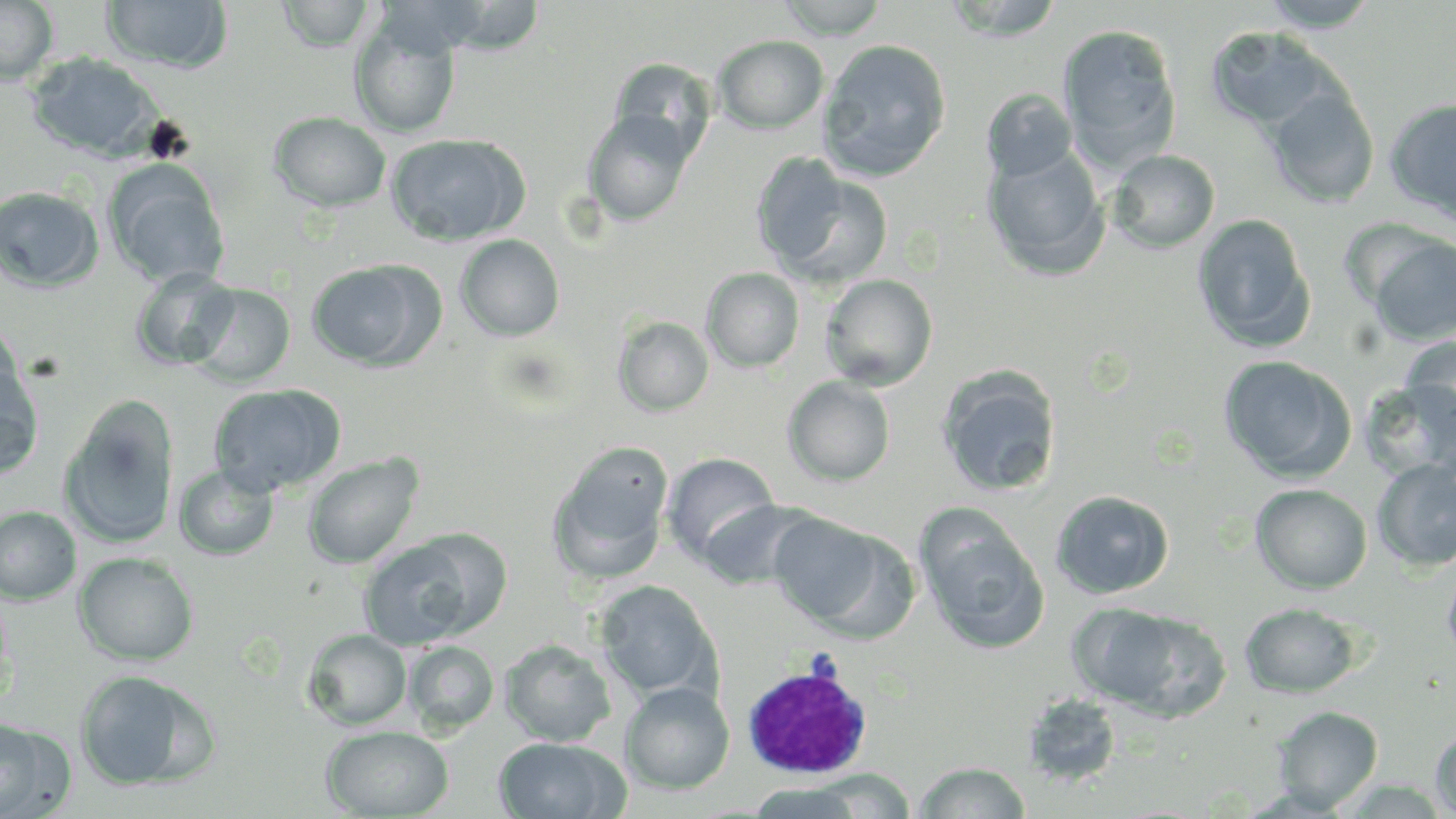

Summary:
  - Coordinate format: approximate bounding boxes as named x1/y1/x2/y2 corners in pixels
  - White blood cell locations: (x1=739, y1=661, x2=876, y2=779)
  - Uninfected red blood cell locations: (x1=0, y1=0, x2=59, y2=87), (x1=775, y1=0, x2=890, y2=39), (x1=940, y1=0, x2=1066, y2=41), (x1=1256, y1=0, x2=1383, y2=32), (x1=100, y1=1, x2=234, y2=73), (x1=277, y1=1, x2=376, y2=52), (x1=349, y1=15, x2=461, y2=138), (x1=1058, y1=23, x2=1182, y2=170), (x1=1206, y1=27, x2=1341, y2=132), (x1=712, y1=35, x2=829, y2=134), (x1=817, y1=38, x2=952, y2=182), (x1=26, y1=53, x2=164, y2=161), (x1=607, y1=58, x2=718, y2=164), (x1=1265, y1=87, x2=1379, y2=209), (x1=982, y1=88, x2=1078, y2=183), (x1=1384, y1=96, x2=1456, y2=224), (x1=583, y1=110, x2=696, y2=227), (x1=268, y1=111, x2=392, y2=212), (x1=385, y1=133, x2=529, y2=246), (x1=983, y1=147, x2=1110, y2=279), (x1=1107, y1=149, x2=1220, y2=253), (x1=752, y1=157, x2=892, y2=290), (x1=104, y1=160, x2=230, y2=288), (x1=0, y1=185, x2=105, y2=292), (x1=1192, y1=214, x2=1316, y2=352), (x1=1364, y1=233, x2=1456, y2=346), (x1=455, y1=234, x2=565, y2=342), (x1=306, y1=258, x2=442, y2=371), (x1=130, y1=267, x2=239, y2=371), (x1=701, y1=267, x2=804, y2=372), (x1=819, y1=274, x2=938, y2=390), (x1=187, y1=282, x2=295, y2=387), (x1=613, y1=316, x2=714, y2=417), (x1=0, y1=320, x2=23, y2=415), (x1=1400, y1=335, x2=1456, y2=443), (x1=1218, y1=355, x2=1357, y2=483), (x1=0, y1=362, x2=45, y2=481), (x1=937, y1=366, x2=1062, y2=498), (x1=1358, y1=375, x2=1456, y2=480), (x1=783, y1=376, x2=896, y2=486), (x1=208, y1=382, x2=345, y2=497), (x1=60, y1=399, x2=179, y2=550), (x1=548, y1=446, x2=675, y2=584), (x1=302, y1=452, x2=424, y2=569), (x1=662, y1=452, x2=779, y2=565), (x1=1372, y1=458, x2=1456, y2=572), (x1=174, y1=464, x2=279, y2=561), (x1=1250, y1=483, x2=1372, y2=594), (x1=1050, y1=490, x2=1174, y2=599), (x1=697, y1=498, x2=819, y2=591), (x1=0, y1=506, x2=82, y2=604), (x1=915, y1=508, x2=1051, y2=655), (x1=767, y1=511, x2=900, y2=634), (x1=407, y1=527, x2=514, y2=636), (x1=359, y1=540, x2=474, y2=652), (x1=74, y1=552, x2=199, y2=666), (x1=1442, y1=561, x2=1456, y2=667), (x1=594, y1=580, x2=719, y2=700), (x1=1239, y1=602, x2=1362, y2=697), (x1=1069, y1=604, x2=1212, y2=715), (x1=303, y1=628, x2=412, y2=730), (x1=500, y1=639, x2=616, y2=746), (x1=404, y1=640, x2=499, y2=735), (x1=74, y1=669, x2=217, y2=792), (x1=620, y1=681, x2=734, y2=795), (x1=1021, y1=693, x2=1123, y2=787), (x1=1271, y1=705, x2=1383, y2=812), (x1=0, y1=718, x2=71, y2=817), (x1=320, y1=725, x2=454, y2=818), (x1=1430, y1=725, x2=1456, y2=818), (x1=494, y1=736, x2=629, y2=819), (x1=915, y1=761, x2=1031, y2=818), (x1=807, y1=768, x2=915, y2=817), (x1=746, y1=782, x2=866, y2=818)
  - Slide-level diagnosis: Plasmodium ovale
  - Image size: 1456×819 pixels
  - Magnification: 1000x
  - Preparation: thin blood film
  - Stain: May-Grünwald-Giemsa
  - Field of view: single
  - Modality: optical microscopy